Classify the preparation.
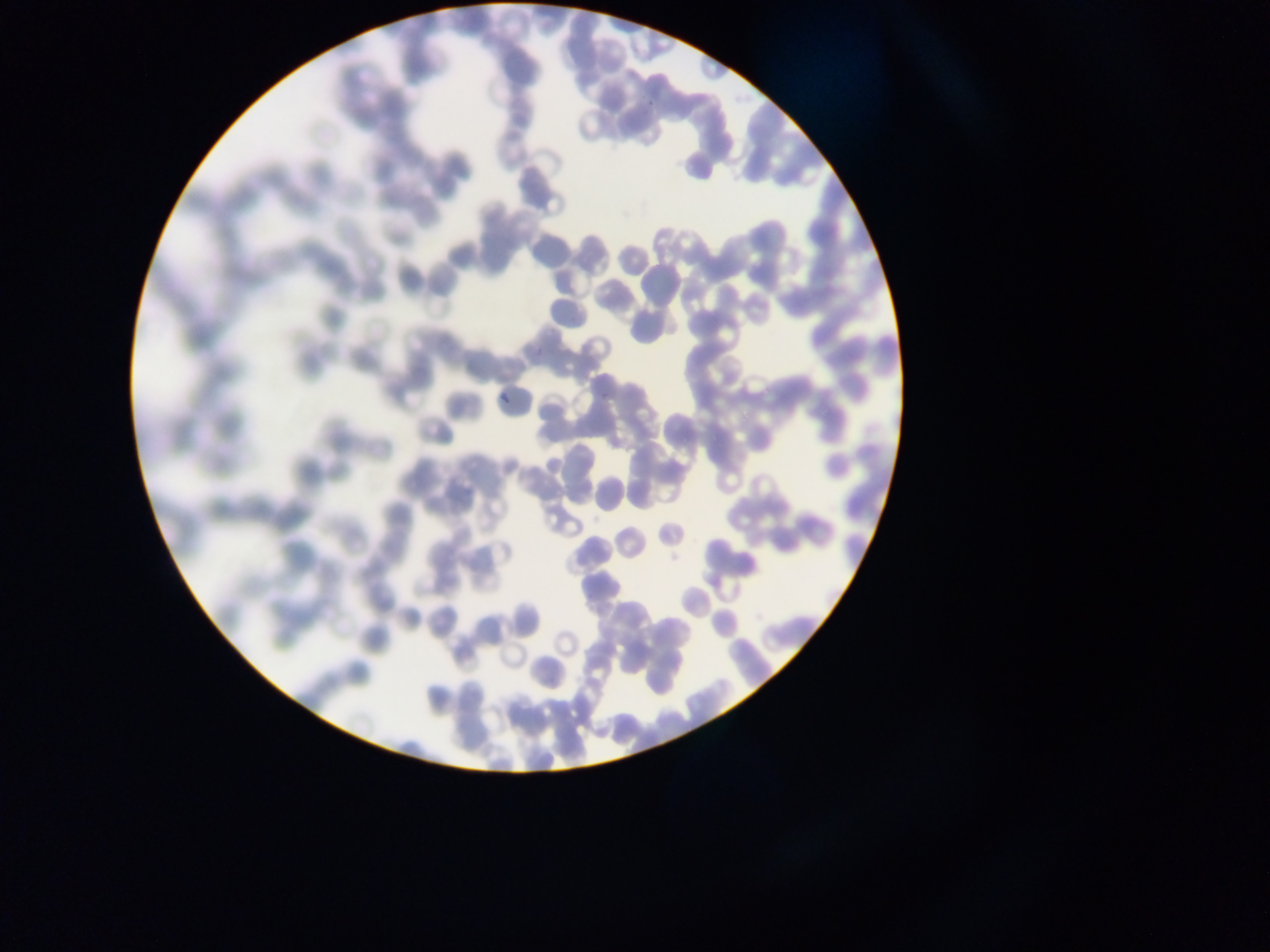
Thin blood film.

{
  "plasmodium_parasite_locations": "approximate bounding boxes as (left, top, right, bottom) in pixels: (493, 391, 510, 403)",
  "capture": "mobile-phone photograph through a microscope",
  "field_of_view": "single",
  "country": "Ghana",
  "image_size": "1270×952 pixels"
}